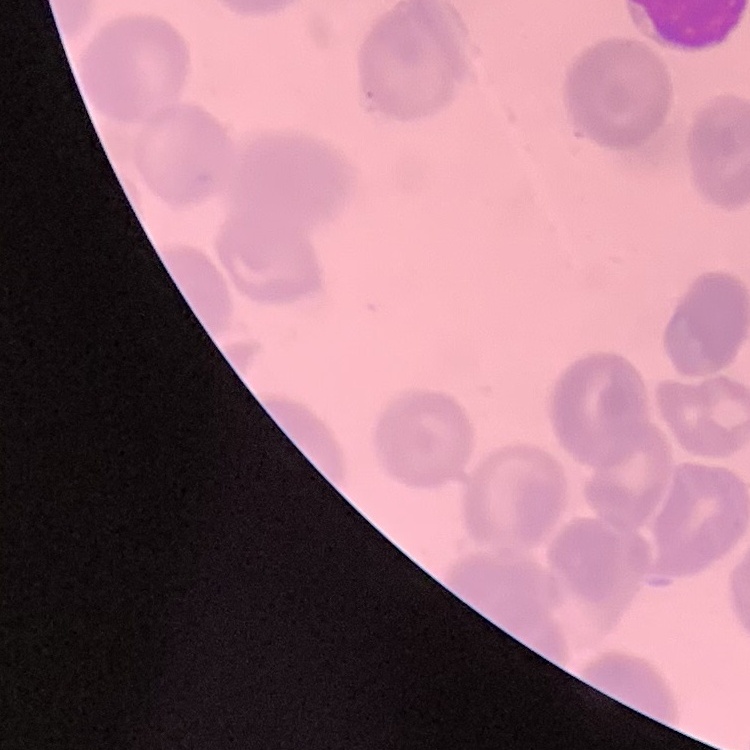 The red blood cells exhibit no rouleaux formation. Stained with either Field's or Giemsa. Thin peripheral smear. One tile cut from a larger photomicrograph.